Locate every Plasmodium parasite.
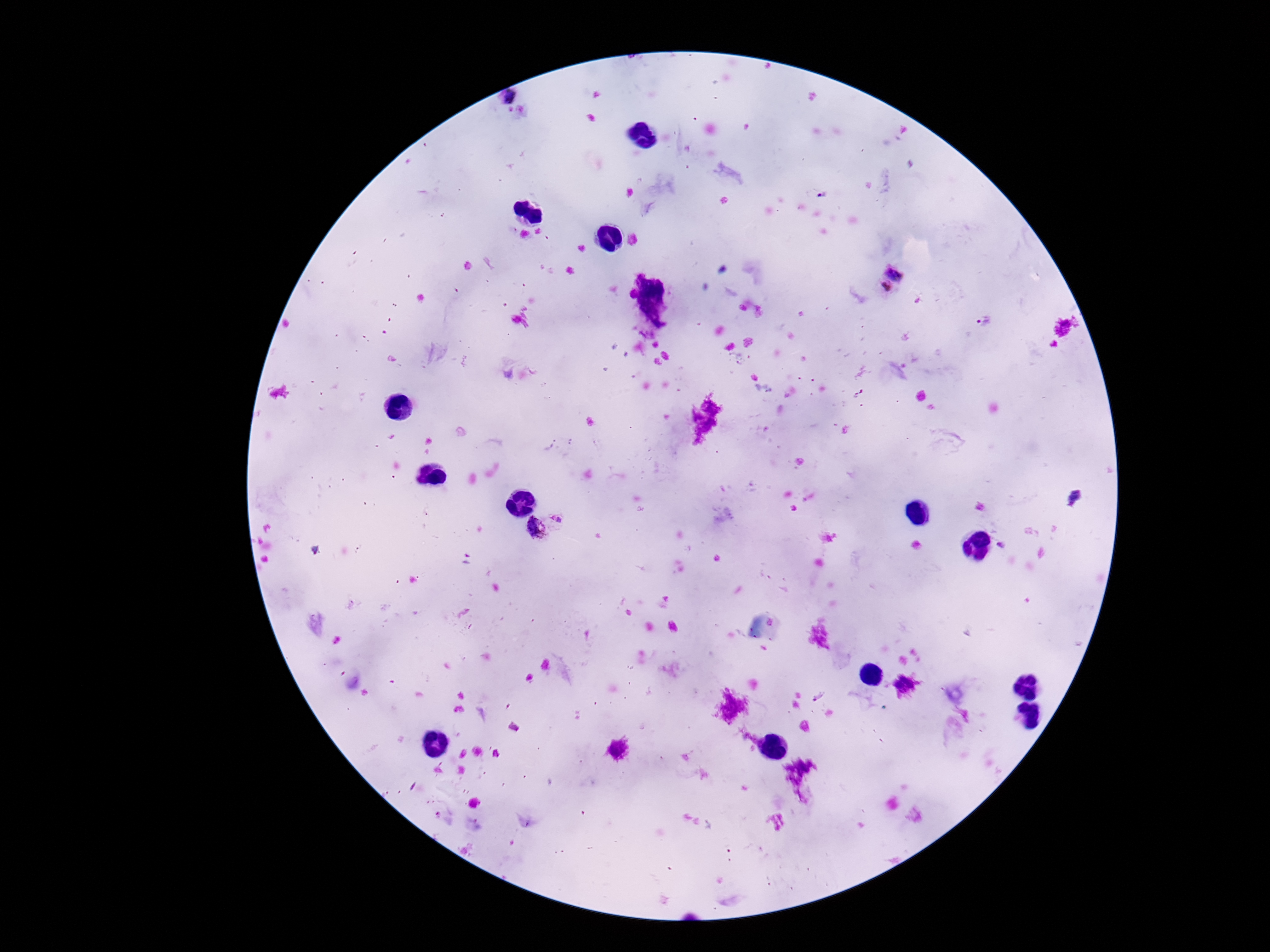

Approximate centers as [x, y] in pixels.
Plasmodium parasites: [510, 95], [888, 280], [982, 321], [558, 516], [536, 528].

Thick blood smear. Smartphone photograph taken through the microscope eyepiece. Image is 1270×952 pixels. 100x magnification. Patient malaria status: positive. Giemsa stain. One field from this slide.